Point out each leukocyte.
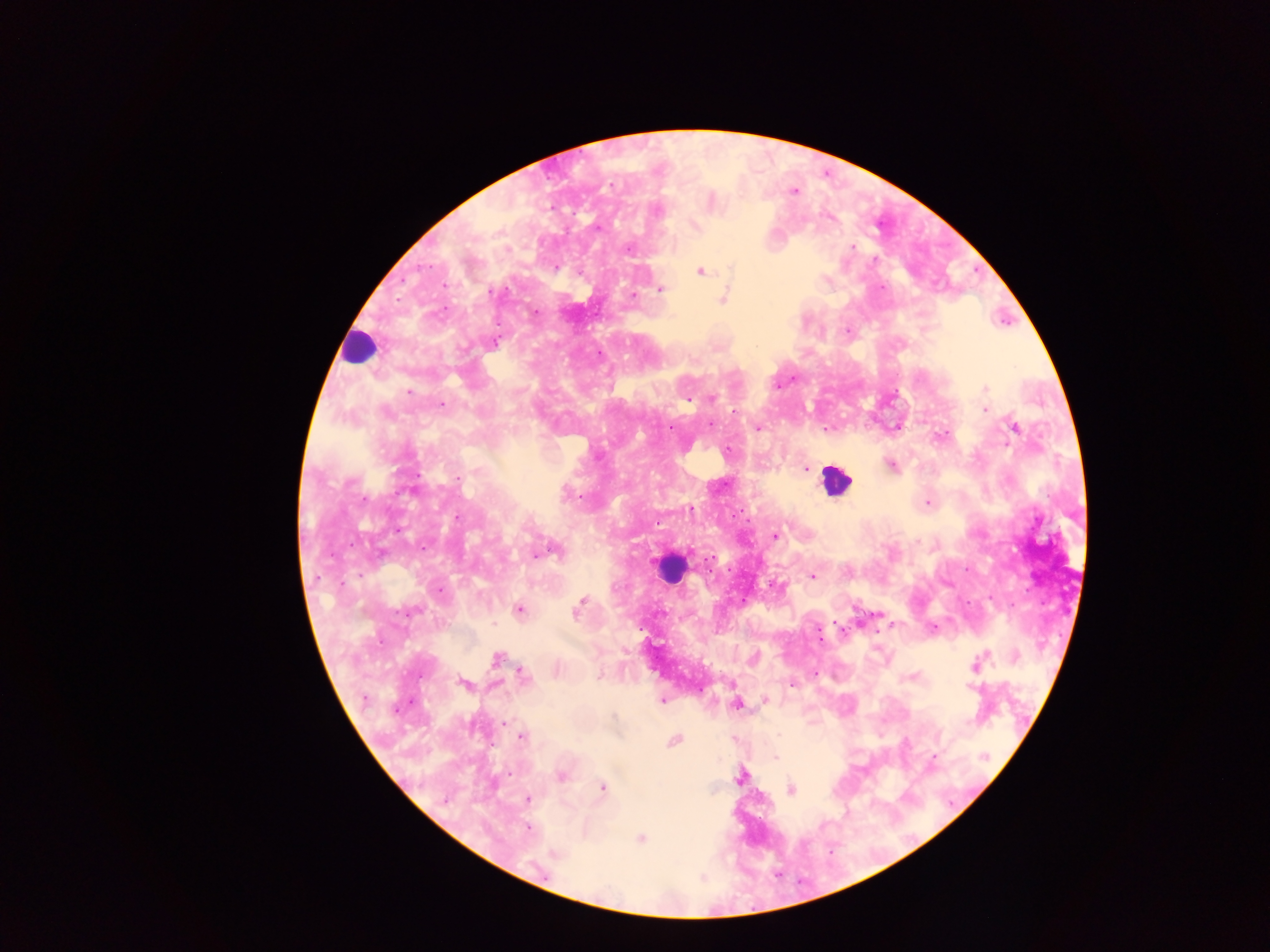
Approximate centers as x y in pixels.
Leukocytes: 359 346; 835 480; 670 568.

Summary:
  - Plasmodium parasite locations: 610 185; 794 192; 657 212; 695 226; 852 247; 628 248; 556 268; 701 272; 661 289; 634 295; 723 299; 536 311; 847 331; 495 342; 985 389; 409 392; 712 399; 687 401; 442 405; 735 410; 985 410; 1014 427; 758 429; 890 465; 805 469; 457 479; 565 495; 573 497; 365 499; 928 503; 690 509; 458 516; 776 535; 555 551; 535 555; 812 576; 440 590; 579 603; 519 610; 410 611; 578 611; 932 627; 820 636; 496 658; 975 665; 523 674; 792 684; 464 685; 364 700; 662 700; 765 700; 736 706; 504 722; 521 737; 674 741; 934 756; 984 756; 776 758; 561 777; 740 778; 603 788; 791 790; 528 799; 528 828; 640 839; 555 854
  - Image size: 1270×952 pixels
  - Country: Ghana
  - Capture: mobile-phone photograph through a microscope
  - Preparation: thick blood smear
  - Field of view: single